Name the cell type shown.
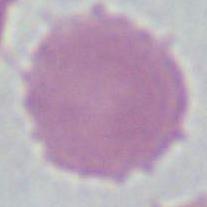
This is an erythrocyte.

Micrograph. Captured at 1000x magnification.